Report the malaria status of this cell.
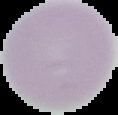
Uninfected.

Summary:
  - Image size: 118×115 pixels
  - Preparation: thin blood film
  - Image type: segmented cell region with the area outside set to black